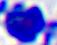
modality = micrograph
identification = leukocyte
magnification = 400x